Identify the blood parasite species.
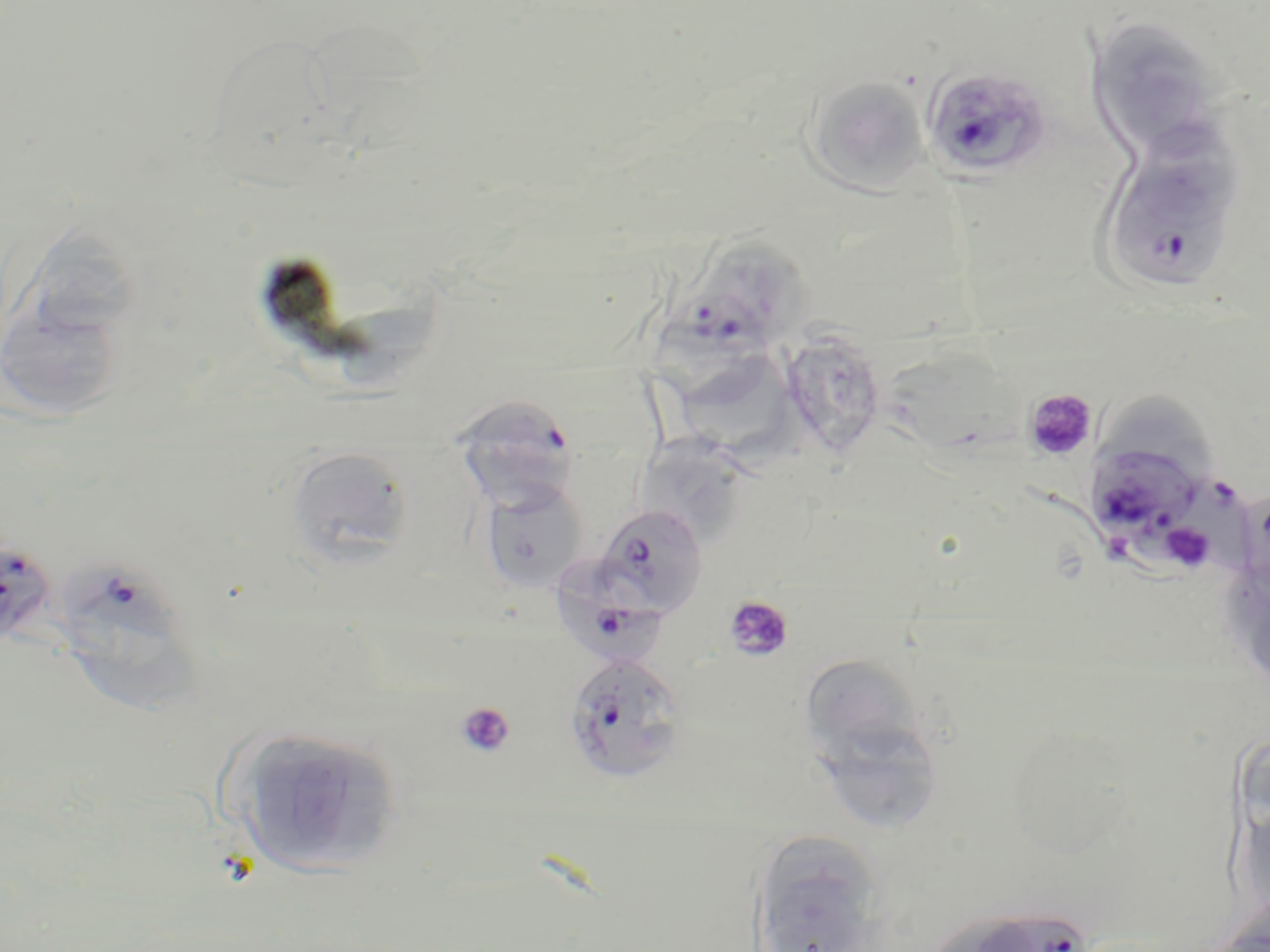
Plasmodium falciparum.

Summary:
  - Coordinate format: approximate bounding boxes as (x1,y1)-(x2,y2) corner pairs in pixels
  - Uninfected red blood cell locations: (1086,18)-(1230,164), (803,76)-(930,195), (23,224)-(150,346), (708,245)-(828,345), (0,294)-(130,424), (325,300)-(444,400), (778,317)-(894,462), (887,339)-(1020,472), (688,356)-(803,500), (1100,382)-(1215,474), (638,437)-(745,548), (286,445)-(415,568), (478,482)-(588,595), (802,659)-(922,760), (825,719)-(943,830), (229,725)-(405,879), (1235,796)-(1270,925), (747,829)-(891,952)
  - Platelet locations: (1023,389)-(1098,464), (1160,522)-(1217,573), (723,595)-(795,662), (455,702)-(516,758)
  - Plasmodium falciparum-infected red blood cell locations: (920,65)-(1054,184), (1096,137)-(1247,296), (648,291)-(772,418), (451,395)-(579,513), (1084,441)-(1211,555), (1177,473)-(1262,607), (591,505)-(709,620), (0,536)-(55,653), (557,556)-(668,670), (65,564)-(210,726), (563,653)-(689,785), (972,905)-(1091,952)
  - Image size: 1270×952 pixels
  - Stain: May-Grünwald-Giemsa
  - Preparation: thin blood smear
  - Field of view: one of a larger specimen
  - Magnification: 1000x
  - Modality: light microscopy